Classify this cell by malaria status.
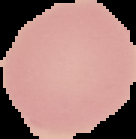
It is uninfected.

Summary:
  - Preparation: thin blood smear
  - Image size: 136×139 pixels
  - Image type: segmented cell region with the area outside set to black